Assess this cell for malaria.
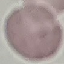

It is uninfected.

Giemsa stain. Cell patch, automatically extracted from a larger field of view and resized to 64 × 64 pixels. Thin blood film. Photographed with a smartphone camera at the microscope eyepiece.